Comment on the morphology of the red blood cells.
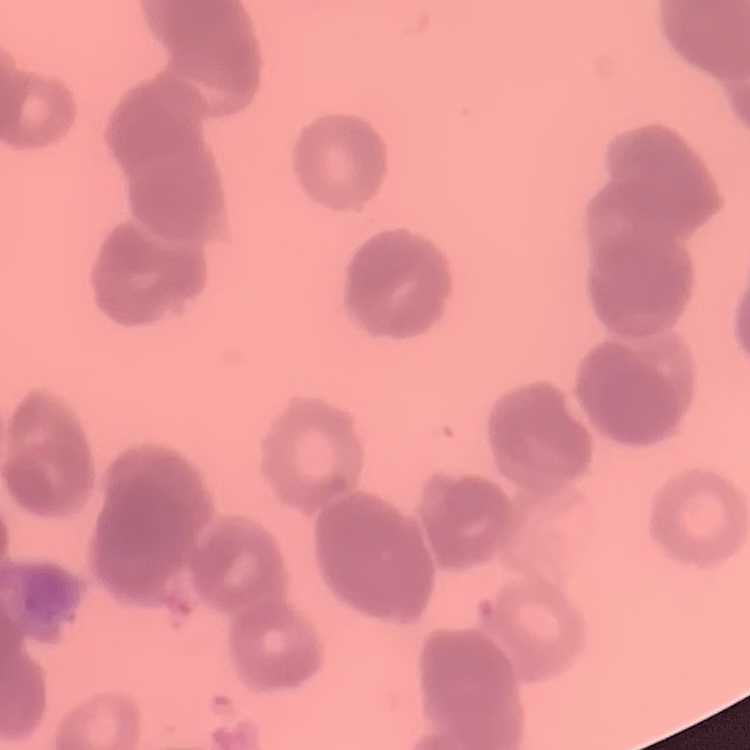
They show rouleaux formation.

preparation: thin peripheral smear
stain: Field's or Giemsa
image_type: square crop of a larger photomicrograph